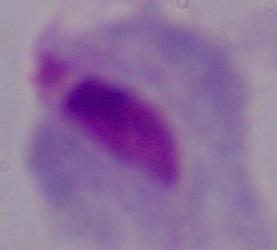 A trichomonad is shown. Micrograph. 1000x magnification.